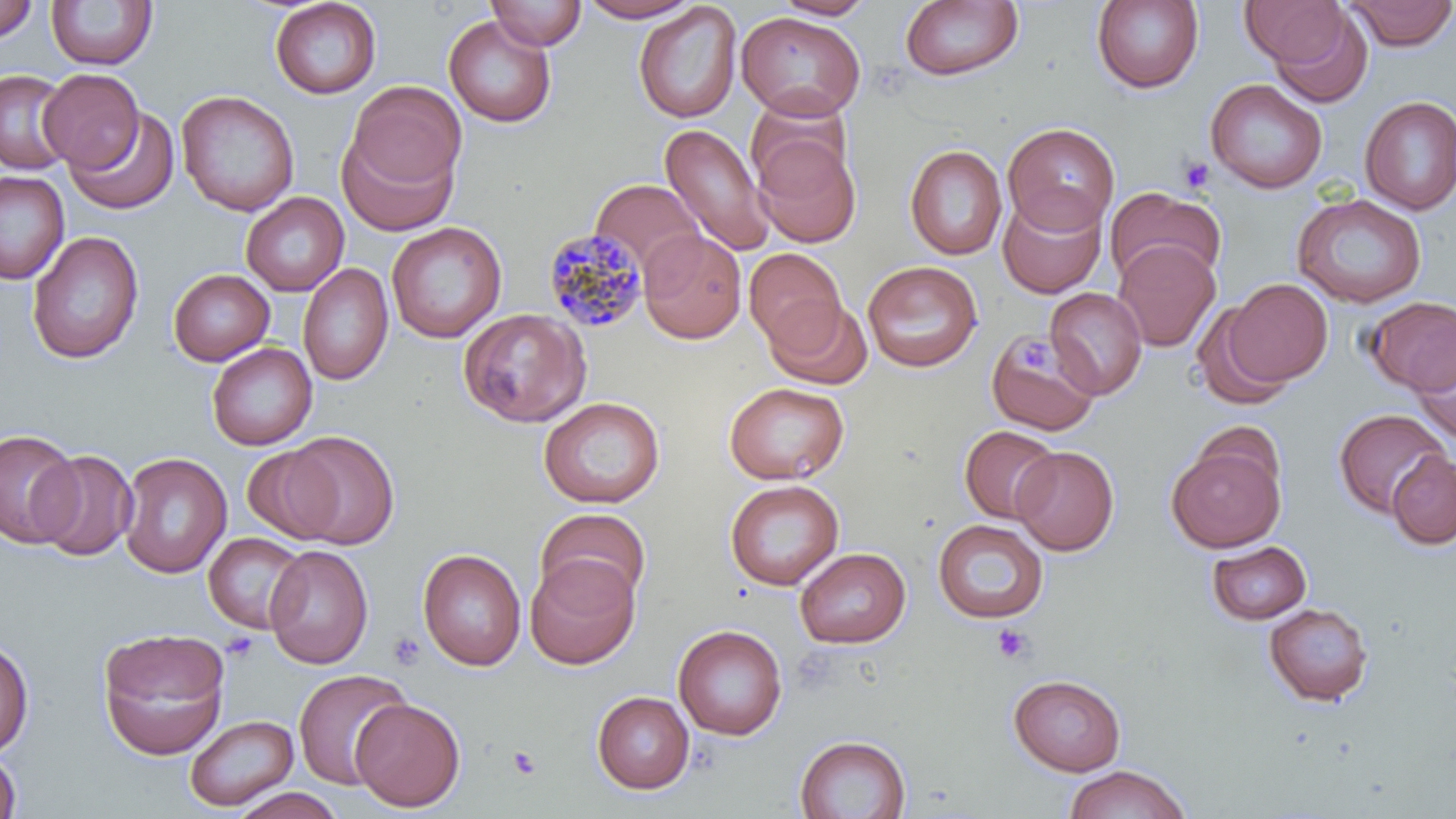

Summary:
  - Coordinate format: approximate bounding boxes as [x1, y1, x2, y2] in pixels
  - Plasmodium malariae-infected red blood cell locations: [541, 228, 650, 334]
  - Uninfected red blood cell locations: [269, 0, 381, 99], [486, 0, 587, 51], [578, 0, 702, 22], [772, 0, 876, 20], [899, 0, 1024, 82], [1091, 0, 1204, 94], [1343, 0, 1456, 50], [0, 1, 39, 42], [46, 1, 157, 71], [1239, 1, 1349, 70], [633, 2, 743, 123], [1265, 8, 1374, 108], [736, 11, 866, 121], [443, 15, 557, 128], [0, 69, 73, 175], [38, 69, 144, 171], [1205, 79, 1327, 194], [346, 80, 468, 195], [176, 90, 299, 216], [745, 96, 852, 195], [1359, 96, 1456, 216], [65, 106, 179, 215], [1002, 122, 1120, 234], [659, 123, 774, 255], [337, 125, 459, 238], [752, 135, 861, 247], [904, 144, 1007, 260], [0, 170, 70, 284], [590, 178, 705, 277], [1105, 186, 1226, 288], [998, 190, 1107, 299], [241, 193, 349, 296], [1292, 193, 1427, 307], [386, 221, 506, 343], [638, 228, 747, 344], [27, 231, 144, 364], [1113, 239, 1220, 352], [744, 248, 847, 353], [862, 261, 983, 372], [297, 263, 394, 386], [168, 268, 274, 366], [1224, 278, 1332, 388], [1044, 287, 1148, 399], [764, 296, 872, 389], [1363, 296, 1456, 395], [1191, 301, 1296, 410], [457, 307, 591, 428], [985, 327, 1100, 435], [1411, 335, 1456, 446], [206, 342, 318, 450], [723, 381, 849, 485], [538, 396, 665, 508], [1333, 408, 1451, 519], [959, 425, 1061, 523], [0, 428, 81, 548], [282, 430, 399, 549], [1166, 442, 1285, 552], [1011, 445, 1119, 555], [242, 446, 344, 543], [32, 449, 139, 562], [1387, 450, 1456, 550], [118, 452, 232, 578], [724, 479, 844, 590], [535, 507, 652, 609], [932, 519, 1048, 624], [203, 532, 307, 634], [1206, 540, 1312, 625], [264, 544, 374, 669], [794, 547, 911, 648], [418, 548, 526, 671], [525, 555, 641, 670], [1263, 602, 1375, 707], [673, 624, 787, 740], [97, 627, 231, 761], [0, 638, 35, 758], [293, 669, 411, 789], [1007, 674, 1128, 776], [592, 691, 694, 794], [350, 698, 466, 811], [185, 714, 299, 812], [794, 734, 911, 818], [0, 748, 22, 819], [1063, 764, 1191, 819], [228, 787, 345, 819]
  - Platelet locations: [1177, 154, 1216, 195], [1018, 337, 1056, 379], [991, 624, 1034, 664], [221, 631, 260, 661], [388, 631, 426, 669], [508, 746, 542, 780]
  - Slide-level diagnosis: Plasmodium malariae
  - Field of view: one of a larger specimen
  - Preparation: thin blood smear
  - Image size: 1456×819 pixels
  - Modality: light microscopy
  - Stain: May-Grünwald-Giemsa
  - Magnification: 1000x